Identify the parasite.
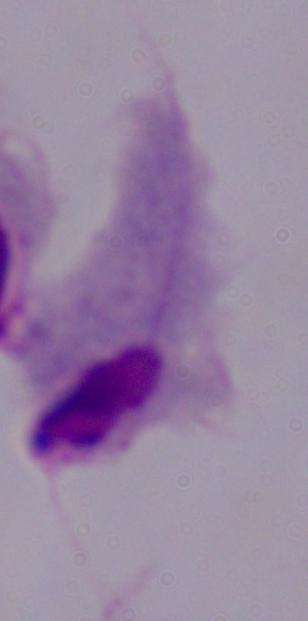

This is a trichomonad.

Photomicrograph. Captured at 1000x magnification.